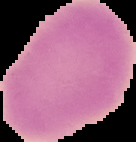

image size = 136×142 pixels
result = no Plasmodium parasites detected
preparation = thin blood film
image type = cell region segmented out of the field of view; surrounding area masked to black